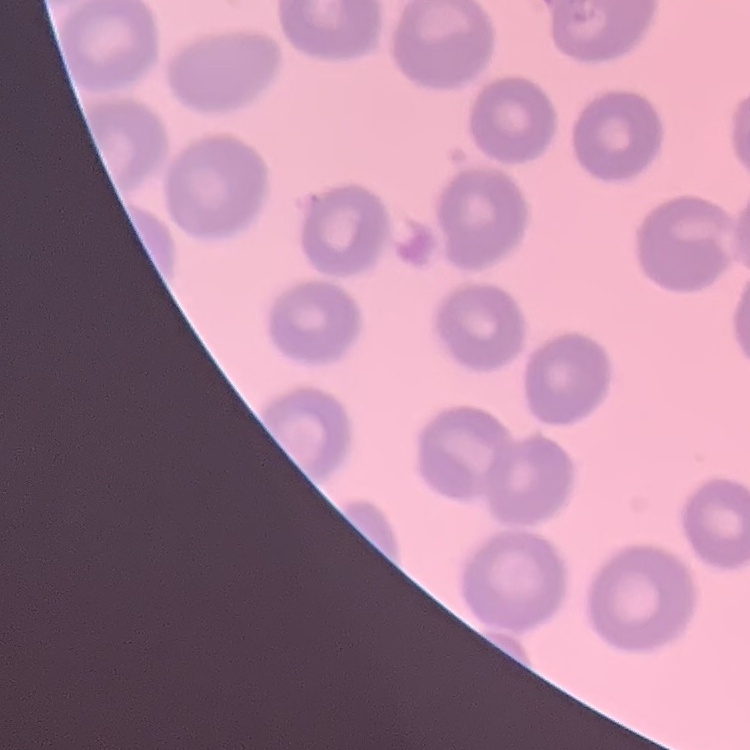

{
  "red_blood_cell_morphology": "no rouleaux formation",
  "preparation": "thin peripheral smear",
  "image_type": "one tile cut from a larger photomicrograph",
  "stain": "Field's or Giemsa"
}